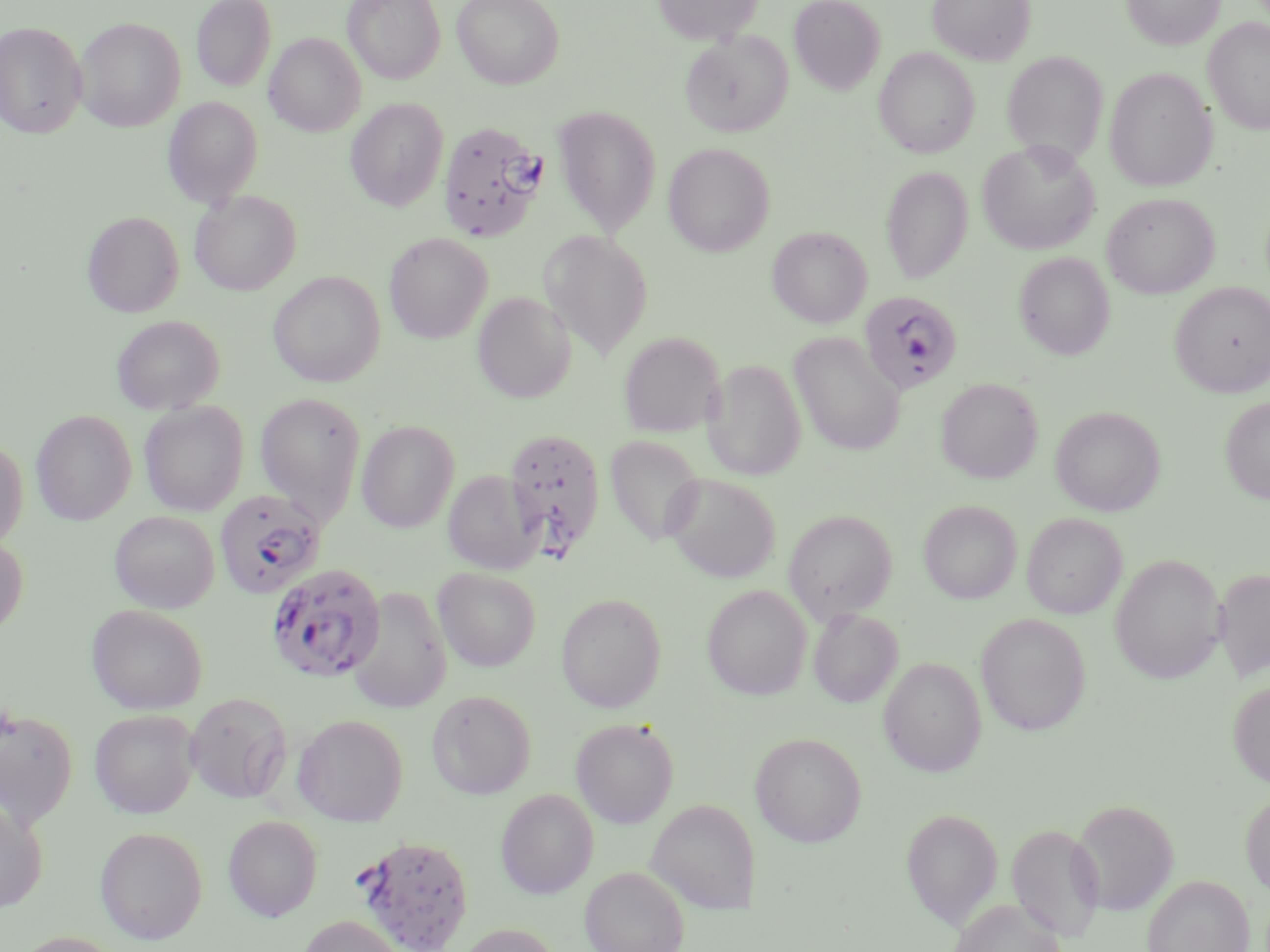 Approximate bounding boxes as (x1,y1)-(x2,y2) corner pairs in pixels. Plasmodium falciparum-infected red blood cell locations: (437,120)-(549,242), (859,291)-(963,396), (504,427)-(605,558), (215,490)-(327,599), (265,563)-(391,684), (356,833)-(474,952). Uninfected red blood cell locations: (191,0)-(276,91), (342,0)-(445,83), (452,0)-(564,89), (652,0)-(764,44), (789,0)-(886,94), (927,0)-(1036,65), (1121,0)-(1224,50), (75,17)-(185,132), (1203,17)-(1270,135), (0,21)-(87,138), (680,31)-(792,137), (265,33)-(365,137), (874,47)-(980,158), (1003,52)-(1108,164), (1104,66)-(1217,192), (163,97)-(262,208), (345,98)-(449,211), (553,106)-(662,235), (977,138)-(1100,255), (663,142)-(775,256), (881,165)-(973,284), (190,190)-(301,295), (1102,192)-(1219,298), (83,211)-(184,317), (767,226)-(872,328), (539,230)-(653,359), (384,232)-(493,343), (1014,252)-(1115,359), (268,271)-(386,387), (1170,281)-(1270,397), (472,292)-(576,403), (112,314)-(225,414), (619,331)-(725,437), (788,332)-(905,455), (703,359)-(805,480), (935,378)-(1043,483), (255,392)-(367,525), (1220,396)-(1270,504), (139,400)-(249,516), (1050,406)-(1166,516), (31,409)-(137,525), (356,420)-(460,533), (604,434)-(706,548), (0,437)-(28,550), (443,469)-(544,575), (664,473)-(781,582), (918,499)-(1022,603), (783,509)-(898,624), (109,511)-(220,613), (1022,513)-(1126,618), (0,534)-(29,639), (1110,553)-(1227,683), (432,567)-(541,671), (1213,567)-(1270,682), (702,584)-(812,700), (348,587)-(452,713), (556,593)-(667,713), (86,604)-(209,714), (808,608)-(902,707), (975,612)-(1091,734), (879,657)-(986,777), (1228,680)-(1270,788), (427,689)-(537,799), (184,692)-(292,804), (0,707)-(78,829), (89,709)-(199,818), (292,714)-(409,826), (571,718)-(679,827), (749,732)-(867,847), (495,788)-(599,899), (1240,789)-(1270,899), (0,797)-(48,913), (645,798)-(760,913), (1070,799)-(1179,915), (901,807)-(1003,929), (223,815)-(323,921), (1007,823)-(1105,941), (94,825)-(208,944), (579,865)-(689,952), (1142,874)-(1254,952), (949,899)-(1066,952), (296,914)-(406,952), (452,923)-(564,952). Slide-level diagnosis: Plasmodium falciparum. Thin blood smear. Light microscopy. May-Grünwald-Giemsa stain. 1000x magnification. Single field of view. Image is 1270×952 pixels.